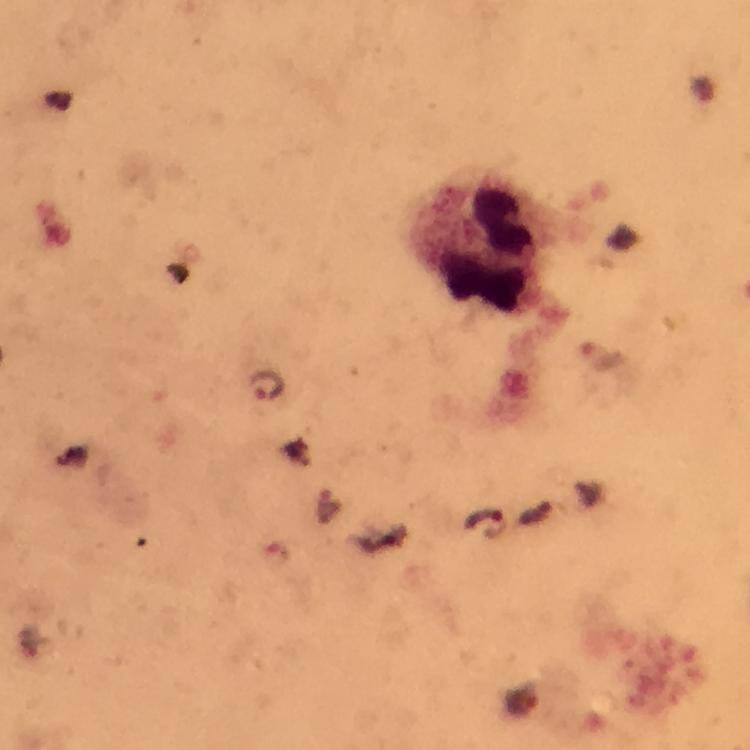
Approximate object centers, in pixels from the top-left corner. Leukocyte locations: (x=482, y=243). Malaria parasite locations: (x=270, y=386), (x=485, y=523). Cropped region of a single field of view. At 100x magnification. Thick smear. Immersion oil was used. Photographed through the microscope with a smartphone camera. Giemsa-stained preparation. Image is 750×750 pixels. From a diagnostic examination for malaria.